Identify the cell.
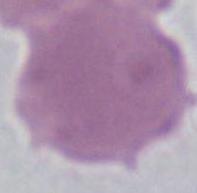
An erythrocyte.

magnification = 1000x
modality = photomicrograph